Classify this cell by malaria status.
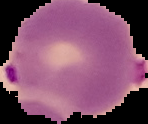

Parasitized.

Summary:
  - Image size: 148×124 pixels
  - Image type: segmented cell region with the area outside set to black
  - Preparation: thin blood film